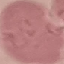

result = negative for malaria parasites
capture = smartphone through the microscope eyepiece
stain = Giemsa
preparation = thin blood film
image type = automatically extracted cell patch, resized to 64 × 64 pixels